Classify this cell by malaria status.
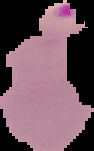

It is parasitized.

Summary:
  - Image size: 94×151 pixels
  - Image type: segmented cell region with the area outside set to black
  - Preparation: thin blood film